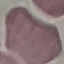
Summary:
  - Malaria status: uninfected
  - Capture: smartphone through the microscope eyepiece
  - Stain: Giemsa
  - Image type: automatically extracted cell patch, resized to 64 × 64 pixels
  - Preparation: thin blood smear